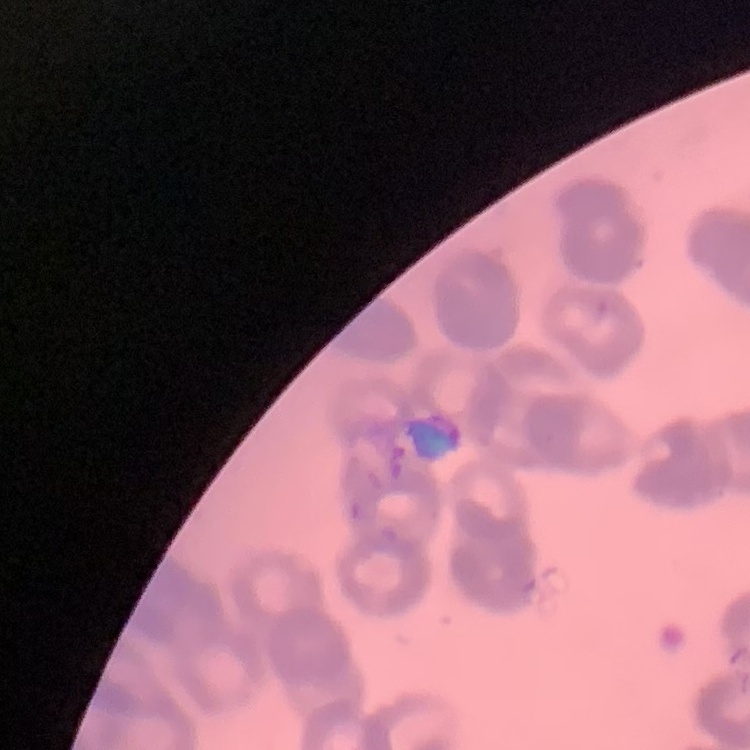 The red blood cells exhibit rouleaux formation. Thin peripheral smear. Field's or Giemsa stain. One tile cut from a larger photomicrograph.